Classify this cell by malaria status.
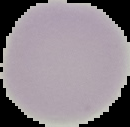
It is uninfected.

The area outside the segmented cell region is set to black. Image is 130×127 pixels. From a thin blood film.